Assess this cell for malaria.
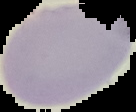

It is uninfected.

Image is 136×112 pixels. From a thin blood film. Cell region segmented out of the field of view; the surrounding area is masked to black.